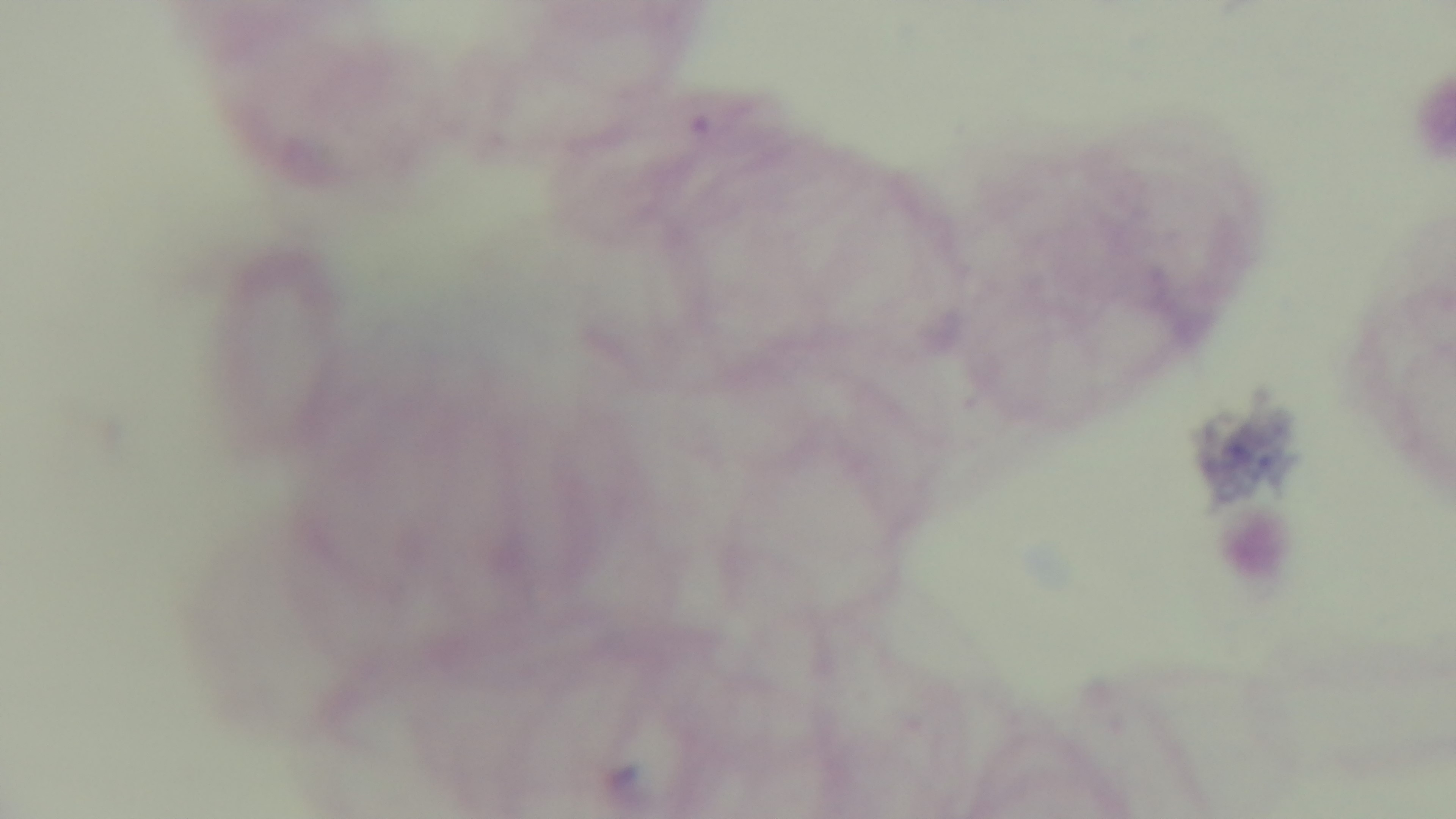

Preparation: thick smear. Oil-immersion objective, 100x. Light microscopy. Giemsa-stained. Malaria status: negative. Captured with a mounted 4K digital camera. Single field of view.